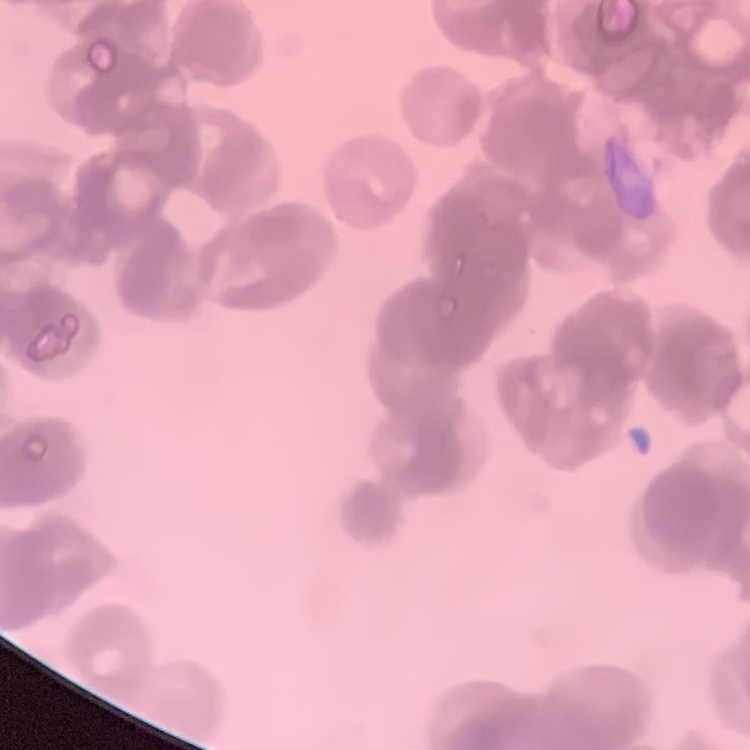
red blood cell morphology = rouleaux formation
image type = one tile cut from a larger photomicrograph
stain = Field's or Giemsa
preparation = thin blood film